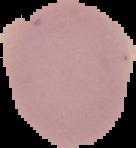
{
  "image_type": "segmented cell region with the area outside set to black",
  "preparation": "thin blood film",
  "result": "no malaria parasites detected",
  "image_size": "136×148 pixels"
}